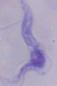
Summary:
  - Identification: trypanosome
  - Magnification: 1000x
  - Modality: photomicrograph